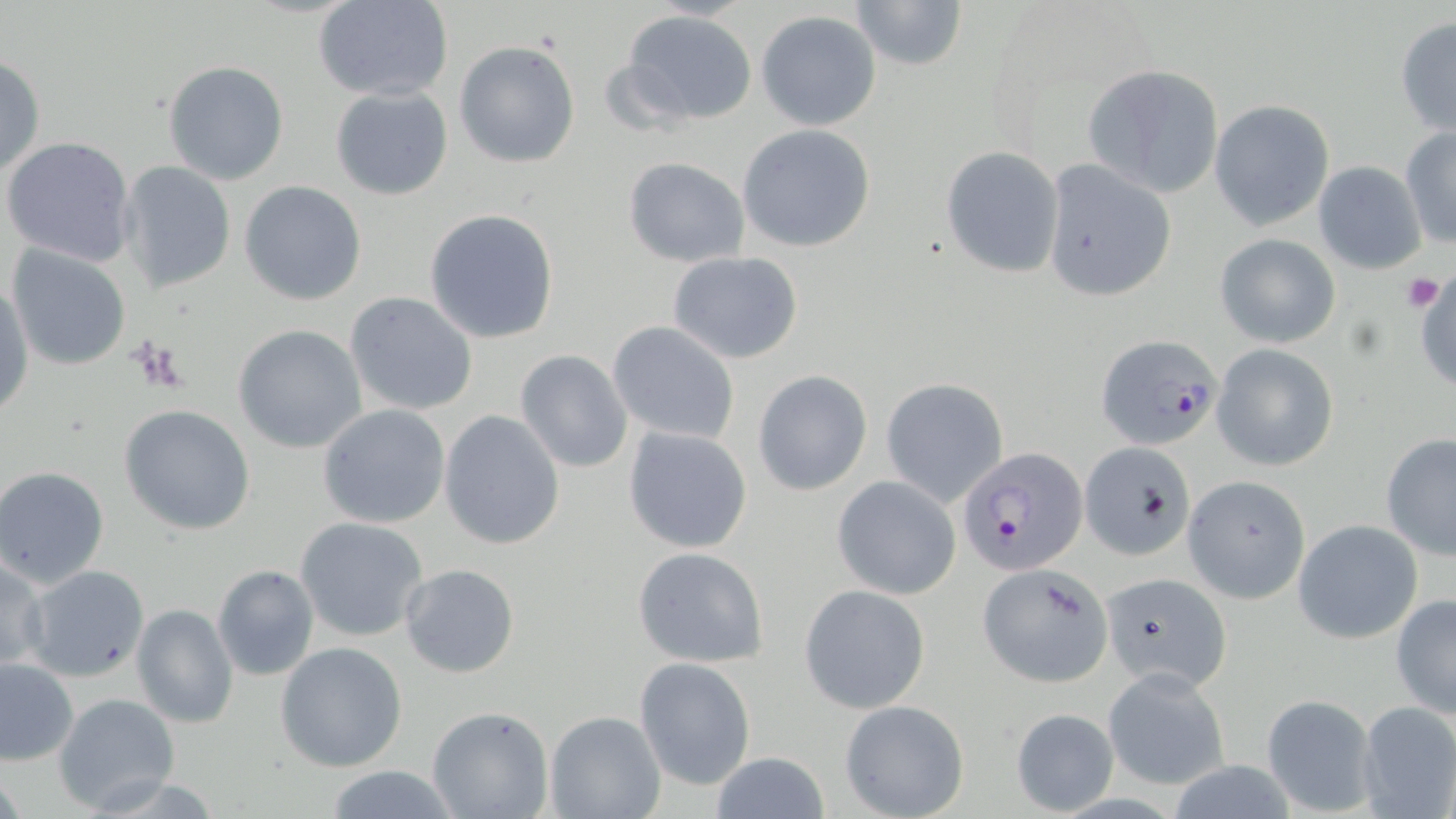

slide_level_diagnosis: Plasmodium falciparum
image_size: 1456×819 pixels
preparation: thin blood smear
platelet_locations: 'approximate bounding boxes as [x1, y1, x2, y2] in pixels: [1399, 273, 1445, 312], [128, 335, 187, 393]'
uninfected_red_blood_cell_locations: 'approximate bounding boxes as [x1, y1, x2, y2] in pixels: [849, 0, 969, 71], [315, 1, 453, 102], [618, 11, 759, 127], [756, 11, 882, 131], [1395, 16, 1456, 136], [453, 41, 581, 168], [0, 53, 46, 180], [162, 61, 290, 185], [1084, 64, 1224, 197], [330, 86, 453, 200], [1210, 100, 1334, 229], [737, 124, 877, 252], [1399, 126, 1456, 250], [2, 136, 138, 268], [941, 146, 1064, 278], [622, 158, 749, 268], [1042, 159, 1177, 303], [116, 160, 237, 296], [1312, 161, 1425, 274], [240, 181, 366, 304], [424, 209, 559, 344], [1215, 233, 1341, 348], [6, 245, 131, 370], [667, 251, 805, 364], [1413, 263, 1456, 396], [1, 281, 33, 412], [344, 291, 478, 415], [608, 322, 739, 445], [233, 325, 368, 452], [1212, 344, 1339, 470], [515, 349, 633, 473], [754, 370, 872, 496], [879, 379, 1011, 508], [317, 404, 451, 529], [118, 405, 256, 535], [439, 409, 566, 550], [623, 426, 753, 554], [1380, 431, 1456, 560], [1081, 442, 1197, 561], [1, 465, 113, 590], [1181, 475, 1310, 604], [833, 476, 961, 600], [295, 517, 431, 644], [1293, 519, 1423, 643], [630, 546, 770, 666], [0, 553, 48, 674], [980, 561, 1113, 684], [20, 564, 151, 683], [213, 564, 318, 680], [399, 564, 521, 679], [1101, 569, 1234, 690], [801, 585, 930, 713], [1391, 594, 1456, 719], [131, 603, 240, 729], [276, 641, 406, 772], [635, 656, 755, 790], [1, 657, 79, 766], [1104, 668, 1229, 790], [52, 692, 181, 814], [1260, 693, 1380, 817], [839, 700, 970, 819], [1355, 701, 1456, 818], [428, 706, 553, 819], [1012, 706, 1120, 814], [545, 711, 665, 819], [707, 752, 833, 819], [321, 765, 460, 819]'
field_of_view: one of a larger specimen
magnification: 1000x
plasmodium_falciparum_infected_red_blood_cell_locations: 'approximate bounding boxes as [x1, y1, x2, y2] in pixels: [1096, 333, 1223, 449], [957, 445, 1086, 577]'
modality: optical microscopy
stain: May-Grünwald-Giemsa